Assess this cell for malaria.
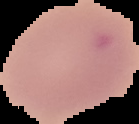

Uninfected.

Cell region segmented out of the field of view; the surrounding area is masked to black. From a thin blood film. Image is 139×124 pixels.